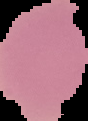

Summary:
  - Image size: 88×121 pixels
  - Result: negative for malaria parasites
  - Preparation: thin blood film
  - Image type: segmented cell region with the area outside set to black